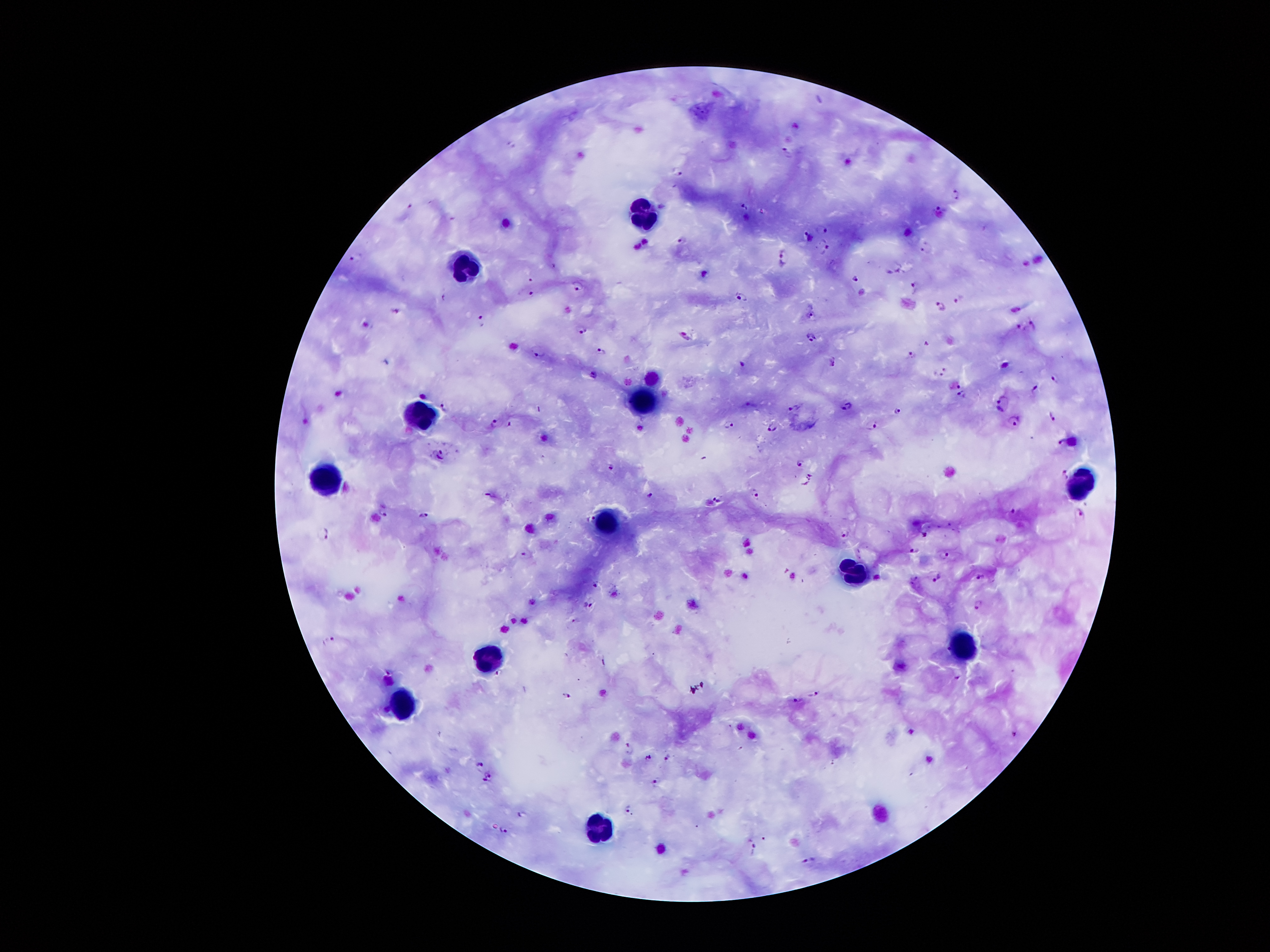
Approximate centers as (x, y) in pixels.
Summary:
  - Leukocyte locations: (639, 219), (470, 269), (642, 408), (421, 412), (328, 487), (1082, 488), (608, 522), (856, 573), (965, 645), (485, 659), (397, 711), (603, 830)
  - Plasmodium parasite locations: (786, 151), (677, 170), (956, 194), (743, 208), (941, 208), (451, 216), (822, 230), (808, 237), (683, 238), (827, 245), (925, 248), (355, 258), (786, 259), (855, 278), (528, 280), (578, 285), (913, 287), (531, 294), (741, 295), (958, 297), (940, 307), (397, 309), (813, 314), (482, 319), (1033, 324), (1018, 327), (582, 328), (686, 336), (810, 337), (926, 342), (602, 350), (538, 353), (912, 354), (833, 362), (743, 364), (942, 372), (1054, 377), (956, 386), (1036, 388), (962, 395), (1003, 401), (445, 406), (795, 407), (846, 407), (898, 411), (1051, 414), (1015, 420), (496, 423), (873, 423), (728, 425), (772, 426), (1063, 441), (441, 455), (800, 461), (610, 465), (1067, 474), (809, 478), (755, 493), (650, 494), (489, 499), (719, 499), (383, 511), (1012, 513), (1081, 513), (424, 514), (844, 532), (326, 534), (923, 534), (915, 550), (527, 555), (946, 556), (938, 577), (979, 577), (597, 584), (589, 603), (977, 603), (331, 638), (499, 671), (391, 672), (815, 693), (565, 695), (794, 699), (629, 748), (667, 755), (647, 757), (480, 763), (488, 776), (656, 779), (626, 807), (521, 813), (502, 828), (754, 846), (811, 859)
  - Capture: smartphone camera through the microscope eyepiece
  - Preparation: thick blood film
  - Magnification: 100x
  - Image size: 1270×952 pixels
  - Stain: Giemsa
  - Field of view: single
  - Patient malaria status: infected with Plasmodium falciparum